Assess this cell for malaria.
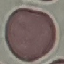
It is uninfected.

Summary:
  - Capture: smartphone through the microscope eyepiece
  - Stain: Giemsa
  - Image type: cell patch, automatically extracted from a larger field of view and resized to 64 × 64 pixels
  - Preparation: thin blood film